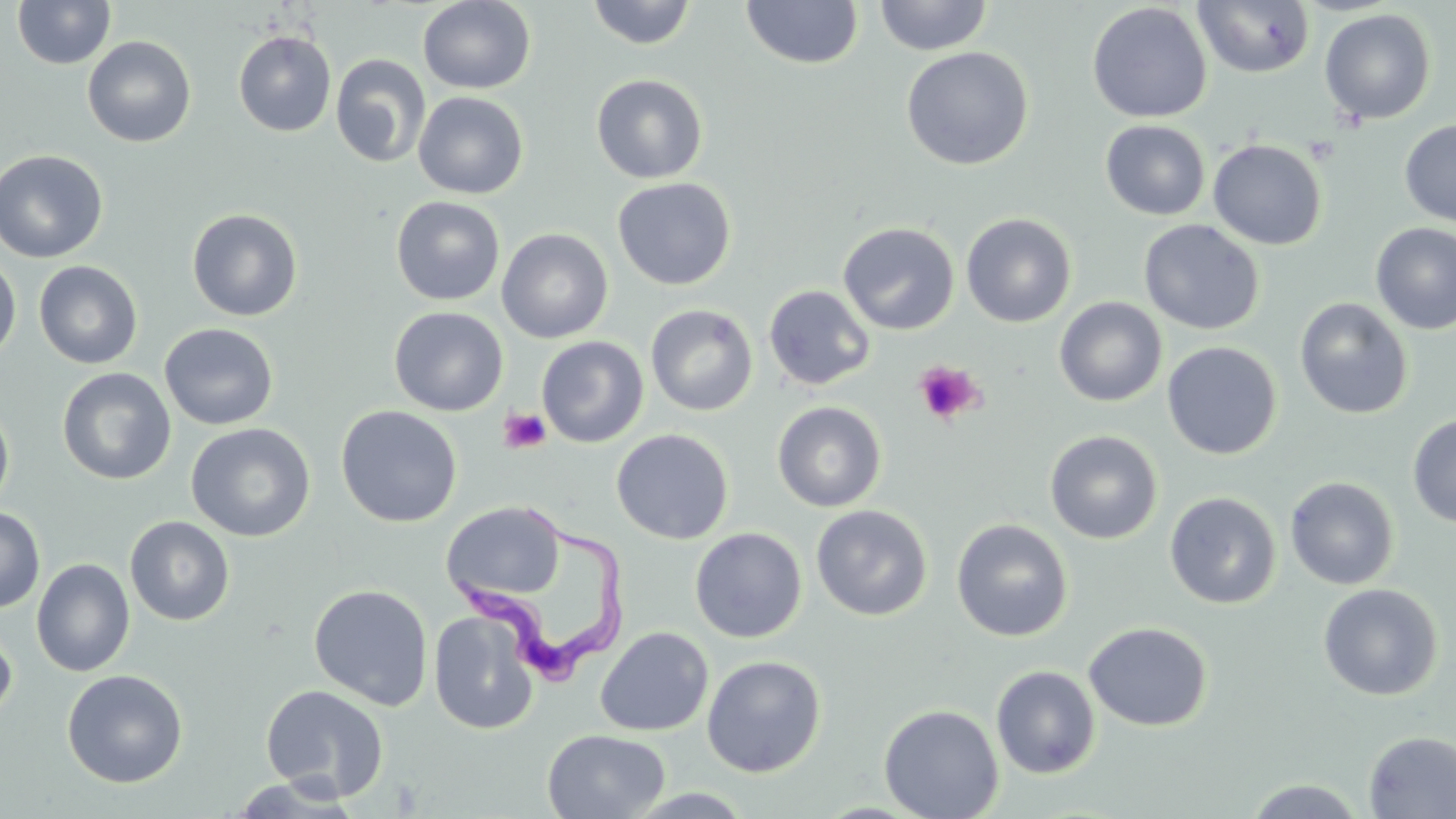
slide-level diagnosis = Trypanosoma brucei
image size = 1456×819 pixels
uninfected red blood cell locations = approximate bounding boxes as [x1, y1, x2, y2] in pixels: [12, 0, 116, 69], [417, 0, 536, 94], [585, 0, 698, 50], [874, 0, 993, 56], [1192, 0, 1315, 79], [741, 1, 863, 70], [1087, 3, 1212, 123], [1319, 9, 1437, 124], [233, 30, 336, 137], [82, 35, 197, 148], [900, 46, 1034, 171], [330, 53, 431, 168], [590, 74, 709, 184], [413, 91, 529, 199], [1100, 119, 1210, 221], [1399, 119, 1456, 227], [1208, 138, 1328, 250], [0, 149, 108, 263], [612, 177, 736, 290], [391, 196, 505, 305], [187, 208, 303, 321], [960, 212, 1077, 328], [1138, 218, 1265, 336], [837, 221, 960, 335], [1370, 223, 1456, 335], [497, 228, 613, 343], [0, 257, 21, 363], [34, 260, 143, 369], [763, 284, 875, 391], [1054, 296, 1167, 407], [1294, 296, 1414, 420], [645, 304, 759, 416], [389, 306, 508, 416], [159, 322, 279, 430], [536, 335, 649, 448], [1162, 341, 1282, 460], [57, 367, 176, 485], [0, 400, 15, 517], [772, 401, 887, 512], [336, 405, 462, 527], [1407, 415, 1456, 527], [186, 422, 316, 542], [611, 428, 734, 544], [1045, 429, 1163, 544], [1284, 476, 1400, 590], [1164, 491, 1282, 609], [441, 501, 566, 604], [811, 504, 933, 621], [0, 507, 45, 614], [125, 515, 235, 626], [951, 518, 1074, 642], [690, 527, 807, 643], [31, 558, 134, 677], [1317, 583, 1443, 701], [308, 584, 433, 710], [429, 609, 539, 735], [1083, 621, 1212, 732], [0, 623, 17, 726], [595, 626, 714, 737], [701, 655, 827, 778], [990, 665, 1101, 779], [62, 669, 188, 788], [260, 684, 390, 800], [879, 704, 1005, 819], [542, 729, 669, 818], [1363, 730, 1456, 818], [226, 775, 363, 817], [1241, 778, 1370, 817], [622, 788, 758, 818]
modality = optical microscopy
stain = May-Grünwald-Giemsa
field of view = single
Trypanosoma brucei locations = approximate bounding boxes as [x1, y1, x2, y2] in pixels: [449, 503, 631, 695]
preparation = thin blood film
platelet locations = approximate bounding boxes as [x1, y1, x2, y2] in pixels: [1303, 135, 1339, 166], [914, 360, 983, 425], [498, 407, 551, 454]
magnification = 1000x